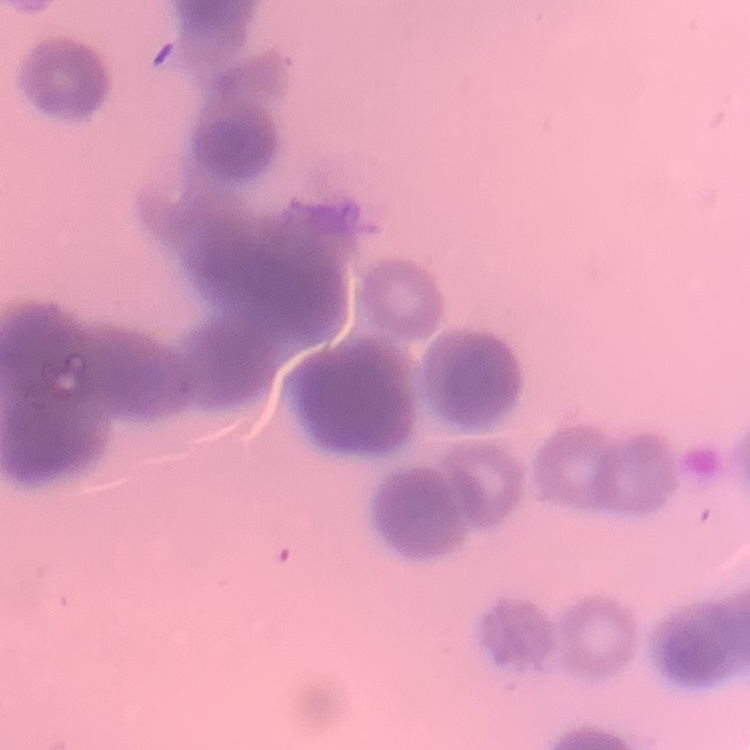
The red blood cells exhibit rouleaux formation. One tile cut from a larger photomicrograph. Stained with either Field's or Giemsa. Thin peripheral smear.